Evaluate for malaria.
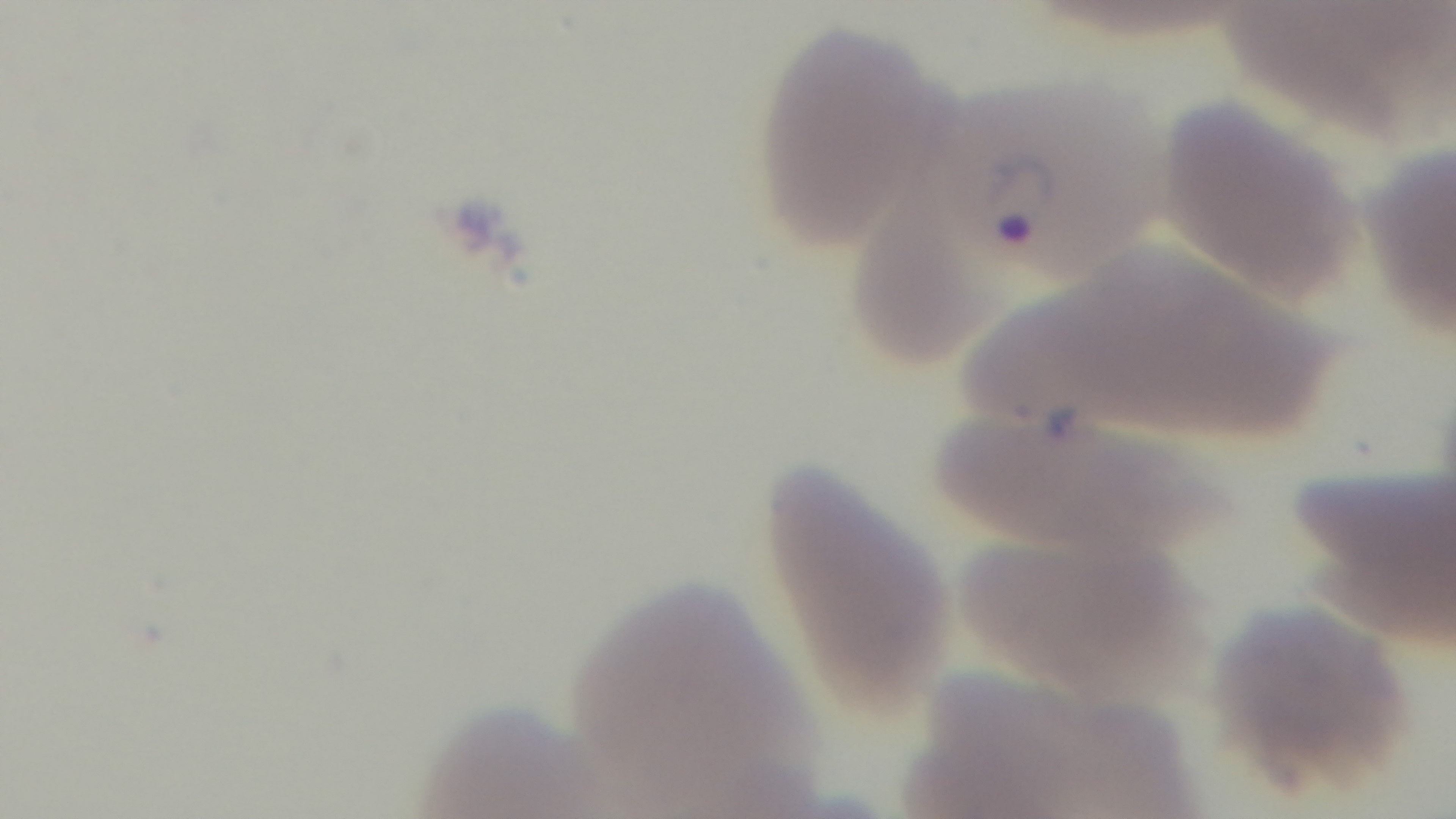

Infected.

Captured with a mounted 4K digital camera. Single field of view. Light microscopy. Oil-immersion objective, 100x. Giemsa stain. Preparation: thin blood film.